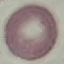
Summary:
  - Malaria status: uninfected
  - Stain: Giemsa
  - Capture: smartphone through the microscope eyepiece
  - Preparation: thin blood film
  - Image type: cell patch, automatically extracted from a larger field of view and resized to 64 × 64 pixels